Identify the cell.
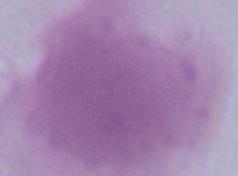
An erythrocyte.

Summary:
  - Magnification: 1000x
  - Modality: photomicrograph